Name the parasite shown.
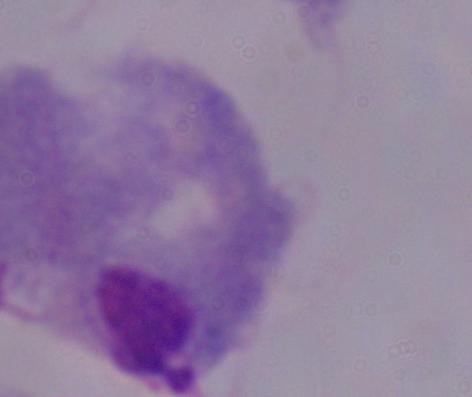
This is a trichomonad.

1000x magnification. Photomicrograph.